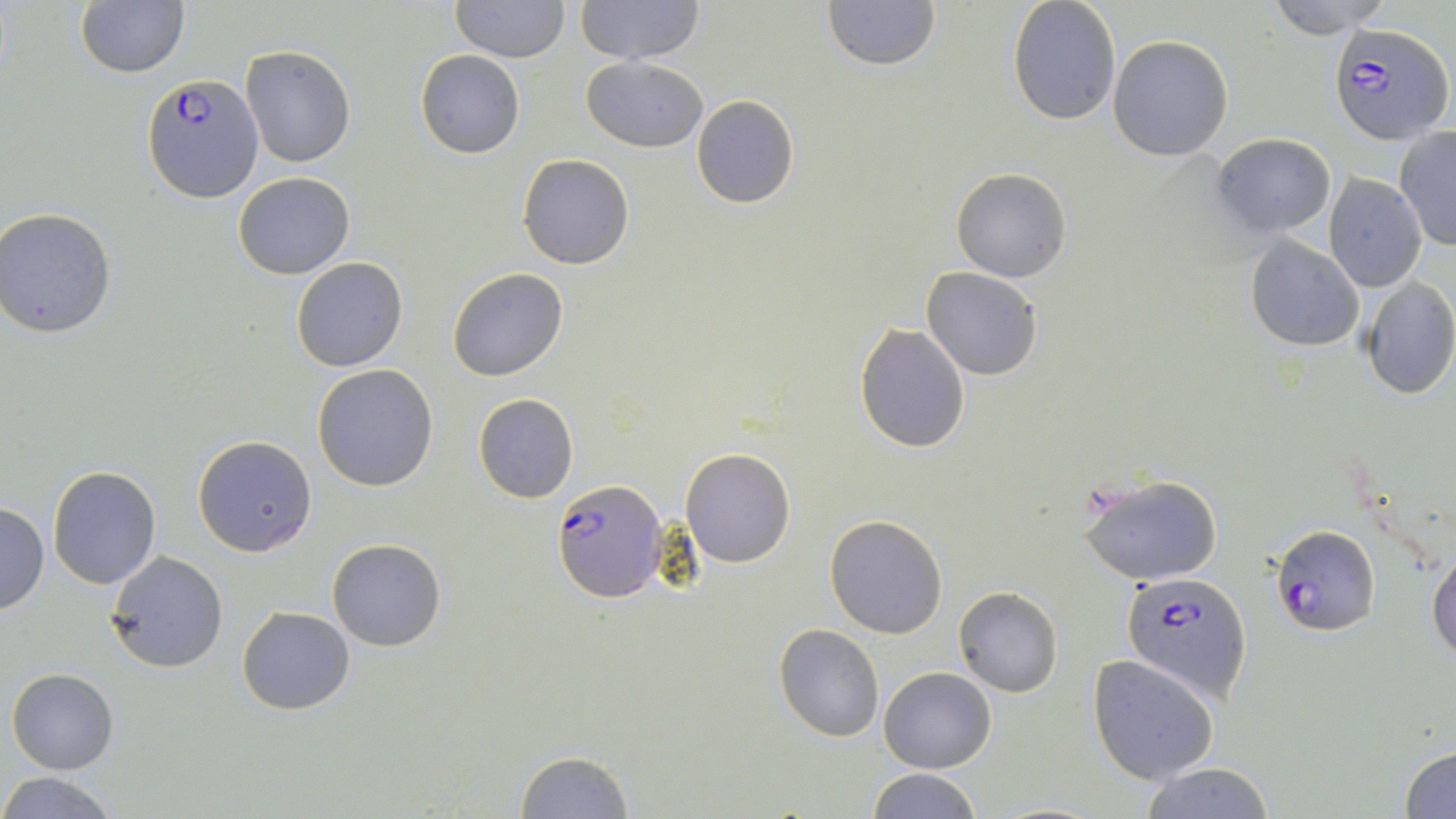

Summary:
  - Coordinate format: approximate bounding boxes as named x1/y1/x2/y2 corners in pixels
  - Uninfected red blood cell locations: (x1=451, y1=0, x2=568, y2=63), (x1=576, y1=0, x2=704, y2=64), (x1=821, y1=0, x2=941, y2=72), (x1=1007, y1=0, x2=1121, y2=123), (x1=1265, y1=0, x2=1394, y2=39), (x1=76, y1=2, x2=189, y2=78), (x1=1108, y1=36, x2=1233, y2=159), (x1=241, y1=45, x2=355, y2=168), (x1=416, y1=49, x2=525, y2=159), (x1=581, y1=57, x2=708, y2=153), (x1=691, y1=95, x2=799, y2=208), (x1=1393, y1=128, x2=1456, y2=251), (x1=1211, y1=133, x2=1335, y2=237), (x1=517, y1=153, x2=635, y2=270), (x1=952, y1=167, x2=1071, y2=282), (x1=233, y1=171, x2=355, y2=279), (x1=1324, y1=174, x2=1427, y2=292), (x1=2, y1=207, x2=119, y2=338), (x1=1244, y1=234, x2=1365, y2=352), (x1=291, y1=257, x2=408, y2=372), (x1=447, y1=267, x2=568, y2=382), (x1=920, y1=267, x2=1043, y2=381), (x1=878, y1=273, x2=1017, y2=417), (x1=1359, y1=275, x2=1456, y2=400), (x1=853, y1=324, x2=971, y2=453), (x1=312, y1=365, x2=439, y2=491), (x1=473, y1=393, x2=579, y2=503), (x1=192, y1=434, x2=318, y2=558), (x1=681, y1=447, x2=795, y2=568), (x1=48, y1=465, x2=161, y2=589), (x1=1077, y1=473, x2=1224, y2=586), (x1=0, y1=503, x2=50, y2=616), (x1=824, y1=515, x2=948, y2=639), (x1=327, y1=538, x2=446, y2=651), (x1=1428, y1=546, x2=1456, y2=659), (x1=104, y1=552, x2=230, y2=673), (x1=954, y1=587, x2=1064, y2=697), (x1=237, y1=606, x2=356, y2=715), (x1=773, y1=623, x2=885, y2=743), (x1=1088, y1=655, x2=1220, y2=785), (x1=879, y1=666, x2=997, y2=773), (x1=7, y1=667, x2=119, y2=775), (x1=1399, y1=742, x2=1456, y2=818), (x1=515, y1=750, x2=633, y2=818), (x1=1138, y1=764, x2=1275, y2=819), (x1=862, y1=767, x2=983, y2=819), (x1=0, y1=772, x2=118, y2=818), (x1=985, y1=802, x2=1112, y2=819)
  - Plasmodium falciparum-infected red blood cell locations: (x1=1330, y1=22, x2=1453, y2=145), (x1=143, y1=74, x2=262, y2=202), (x1=553, y1=478, x2=667, y2=603), (x1=1271, y1=525, x2=1380, y2=636), (x1=1120, y1=571, x2=1252, y2=704)
  - Slide-level diagnosis: Plasmodium falciparum
  - Image size: 1456×819 pixels
  - Magnification: 1000x
  - Preparation: thin blood smear
  - Field of view: one of a larger specimen
  - Modality: optical microscopy
  - Stain: May-Grünwald-Giemsa